Give the extent of all Plasmodium vivax-infected red blood cells.
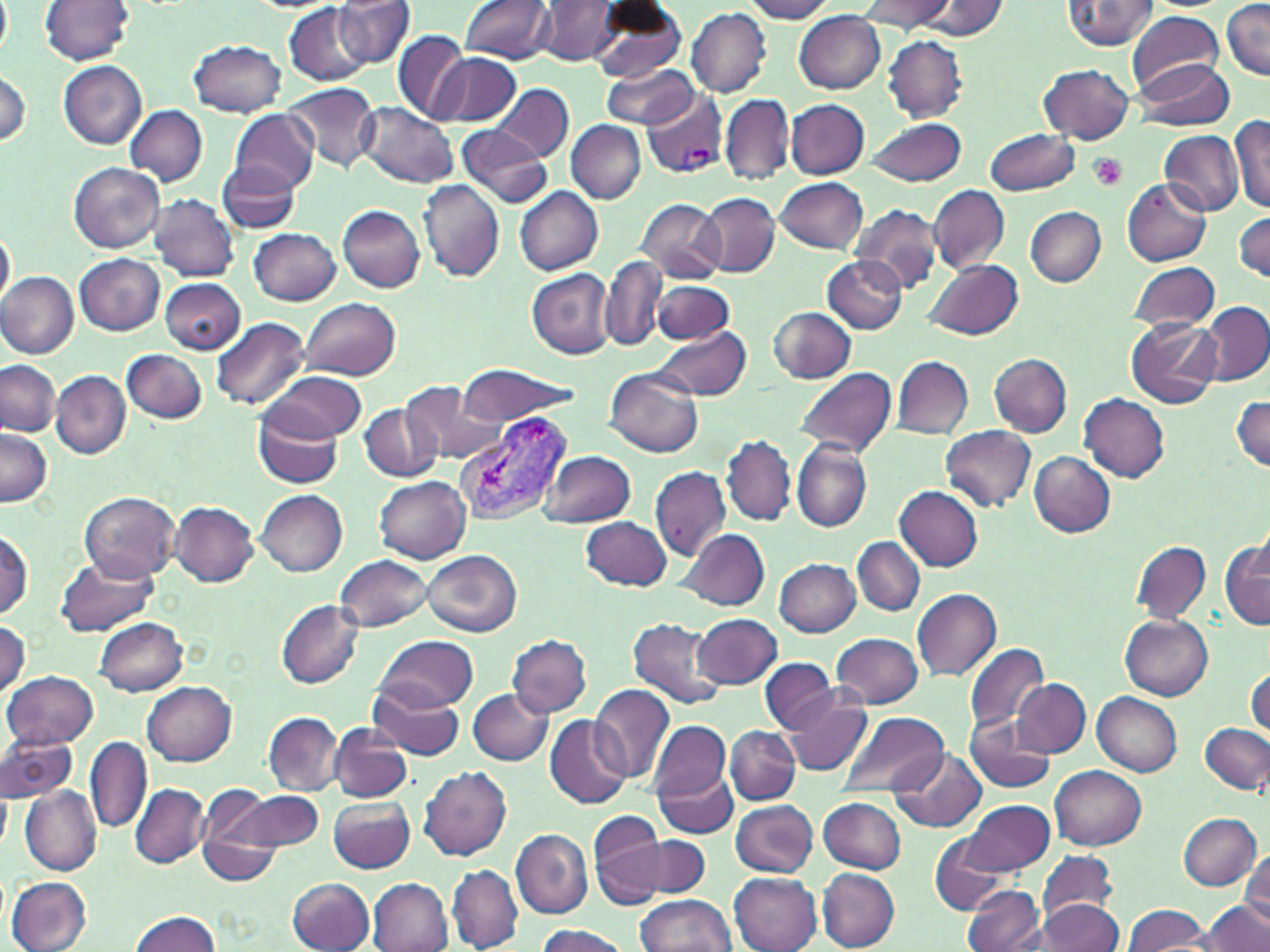

Approximate bounding boxes as (x1, y1, x2, y2) in pixels.
Plasmodium vivax-infected red blood cells: (641, 88, 727, 179), (455, 411, 575, 525).

Summary:
  - Platelet locations: (1087, 153, 1128, 192)
  - Uninfected red blood cell locations: (0, 0, 11, 59), (40, 0, 134, 64), (335, 0, 416, 70), (460, 0, 556, 63), (537, 0, 620, 66), (589, 0, 689, 82), (741, 0, 838, 22), (858, 0, 955, 33), (1063, 0, 1159, 50), (916, 1, 1010, 39), (1221, 2, 1268, 81), (285, 3, 373, 84), (686, 6, 771, 97), (794, 11, 886, 93), (1127, 11, 1223, 94), (393, 29, 469, 124), (882, 36, 967, 121), (188, 39, 286, 117), (431, 52, 520, 127), (1130, 59, 1234, 130), (59, 60, 148, 148), (1039, 64, 1135, 143), (601, 65, 700, 130), (0, 68, 32, 148), (493, 83, 573, 160), (284, 84, 380, 171), (720, 92, 794, 187), (786, 99, 869, 179), (359, 102, 459, 188), (124, 105, 207, 186), (232, 110, 318, 194), (1230, 116, 1270, 213), (866, 118, 967, 186), (568, 121, 646, 203), (457, 124, 551, 207), (985, 129, 1082, 196), (1159, 129, 1244, 217), (219, 160, 300, 233), (69, 162, 164, 252), (775, 177, 867, 253), (1121, 178, 1211, 266), (417, 180, 504, 281), (929, 185, 1009, 272), (515, 187, 603, 275), (690, 190, 861, 267), (697, 193, 779, 277), (148, 194, 239, 281), (635, 198, 725, 283), (851, 203, 944, 294), (337, 205, 425, 293), (1026, 207, 1105, 287), (1233, 212, 1269, 282), (0, 226, 16, 310), (250, 226, 342, 305), (75, 253, 165, 335), (822, 255, 907, 334), (601, 257, 667, 353), (925, 257, 1022, 340), (1129, 262, 1221, 333), (526, 269, 615, 358), (0, 271, 78, 358), (159, 277, 245, 354), (653, 280, 734, 344), (300, 297, 400, 382), (1201, 301, 1270, 384), (769, 307, 857, 383), (211, 317, 312, 412), (1126, 317, 1221, 409), (651, 326, 752, 401), (122, 349, 207, 423), (989, 353, 1071, 436), (892, 355, 973, 439), (1, 360, 61, 437), (456, 365, 580, 425), (794, 367, 897, 458), (604, 368, 703, 457), (51, 370, 130, 458), (267, 370, 366, 440), (401, 380, 502, 464), (1078, 393, 1170, 483), (1231, 396, 1270, 472), (359, 402, 441, 482), (253, 404, 343, 489), (941, 425, 1037, 512), (1, 428, 53, 506), (723, 435, 797, 526), (792, 440, 872, 532), (1029, 451, 1116, 538), (540, 452, 635, 528), (650, 466, 731, 561), (375, 476, 470, 563), (895, 485, 983, 570), (255, 490, 347, 577), (79, 491, 181, 583), (170, 501, 259, 586), (581, 515, 671, 590), (679, 528, 769, 610), (0, 530, 34, 620), (853, 537, 924, 615), (1133, 539, 1211, 624), (1220, 540, 1269, 629), (422, 549, 521, 638), (334, 554, 432, 633), (56, 557, 159, 637), (774, 558, 861, 637), (913, 589, 1002, 681), (276, 599, 365, 689), (692, 613, 782, 689), (1121, 615, 1213, 700), (93, 616, 188, 696), (626, 617, 726, 709), (0, 619, 30, 697), (833, 632, 923, 707), (372, 634, 479, 717), (506, 634, 591, 717), (963, 641, 1049, 733), (759, 658, 838, 734), (1246, 667, 1269, 738), (5, 671, 99, 750), (1013, 679, 1090, 756), (141, 680, 237, 766), (589, 683, 676, 783), (371, 685, 468, 760), (468, 688, 553, 767), (1092, 692, 1181, 776), (785, 693, 873, 776), (837, 709, 949, 797), (264, 712, 343, 795), (966, 713, 1054, 792), (546, 714, 631, 809), (649, 721, 730, 806), (1200, 723, 1270, 793), (329, 724, 412, 802), (725, 726, 799, 803), (0, 730, 79, 805), (86, 736, 152, 833), (655, 763, 737, 839), (1051, 764, 1147, 848), (420, 766, 511, 862), (889, 770, 987, 830), (130, 783, 209, 868), (0, 785, 11, 853), (20, 785, 101, 875), (194, 787, 288, 886), (228, 790, 323, 856), (328, 796, 415, 874), (819, 797, 907, 873), (958, 798, 1053, 877), (730, 800, 818, 877), (589, 811, 664, 910), (1177, 814, 1261, 890), (511, 829, 592, 919), (652, 836, 713, 895), (929, 836, 1011, 913), (1038, 848, 1118, 926), (1239, 850, 1269, 932), (446, 864, 523, 952), (818, 867, 900, 950), (729, 872, 821, 952), (8, 877, 91, 952), (286, 877, 374, 952), (368, 878, 451, 951), (963, 886, 1043, 952), (637, 894, 736, 952), (1035, 900, 1123, 951), (1201, 900, 1269, 952), (1122, 903, 1211, 952), (128, 910, 222, 952), (534, 924, 629, 952)
  - Slide-level diagnosis: Plasmodium vivax
  - Modality: light microscopy
  - Field of view: one of a larger specimen
  - Magnification: 1000x
  - Stain: May-Grünwald-Giemsa
  - Image size: 1270×952 pixels
  - Preparation: thin blood smear